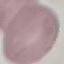

malaria status = uninfected
image type = cell patch, automatically extracted from a larger field of view and resized to 64 × 64 pixels
stain = Giemsa
preparation = thin blood film
capture = smartphone camera at the microscope eyepiece